Locate and identify every blood parasite.
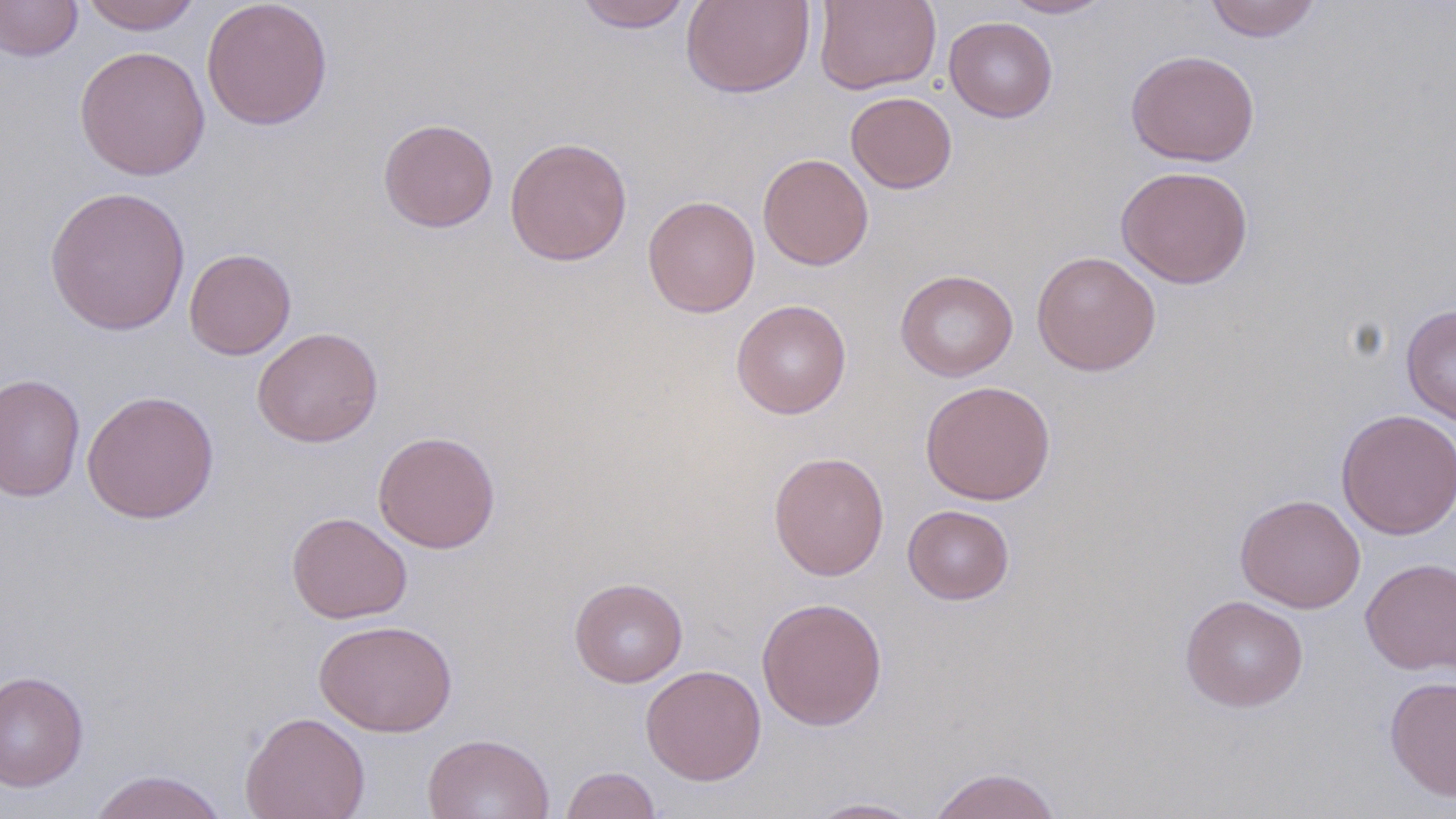
No blood parasites observed.

slide_level_diagnosis: no evidence of blood parasites
field_of_view: one of a larger specimen
magnification: 1000x
preparation: thin blood film
uninfected_red_blood_cell_locations: 'approximate bounding boxes as (x1,y1)-(x2,y2) corner pairs in pixels: (80,0)-(202,34), (201,0)-(333,130), (680,0)-(815,98), (814,0)-(941,94), (1003,0)-(1114,18), (1204,0)-(1323,42), (0,1)-(82,62), (575,1)-(693,32), (944,16)-(1058,123), (74,45)-(211,181), (1125,48)-(1260,167), (845,91)-(958,194), (378,118)-(498,233), (504,136)-(633,267), (757,153)-(873,270), (1116,165)-(1254,288), (44,185)-(192,336), (643,195)-(760,317), (184,248)-(296,360), (1031,250)-(1162,376), (895,269)-(1018,382), (731,299)-(851,419), (1401,304)-(1456,425), (251,326)-(383,448), (0,373)-(85,503), (920,380)-(1056,505), (81,389)-(219,524), (1336,408)-(1456,541), (372,431)-(501,553), (768,450)-(889,581), (1235,493)-(1366,613), (902,504)-(1015,605), (286,512)-(412,624), (1360,557)-(1456,675), (569,577)-(688,687), (1180,594)-(1308,712), (756,596)-(888,730), (314,618)-(458,737), (641,664)-(767,786), (0,670)-(90,793), (1384,674)-(1456,802), (239,711)-(370,819), (422,732)-(555,819), (560,766)-(661,819), (928,766)-(1063,819), (88,769)-(230,819), (802,797)-(929,818)'
image_size: 1456×819 pixels
stain: May-Grünwald-Giemsa
modality: optical microscopy